Identify the parasite.
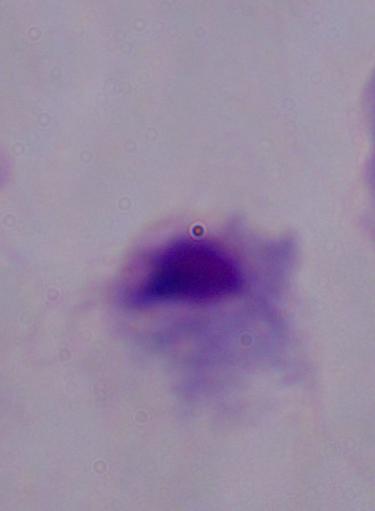

A trichomonad.

Summary:
  - Modality: micrograph
  - Magnification: 1000x